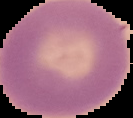

preparation = thin blood film
image size = 133×118 pixels
image type = cell region segmented out of the field of view; surrounding area masked to black
malaria status = uninfected